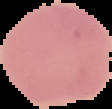 Image is 112×109 pixels. Cell region segmented out of the field of view; the surrounding area is masked to black. Result: no Plasmodium parasites detected. From a thin blood film.